Give the position of every malaria parasite.
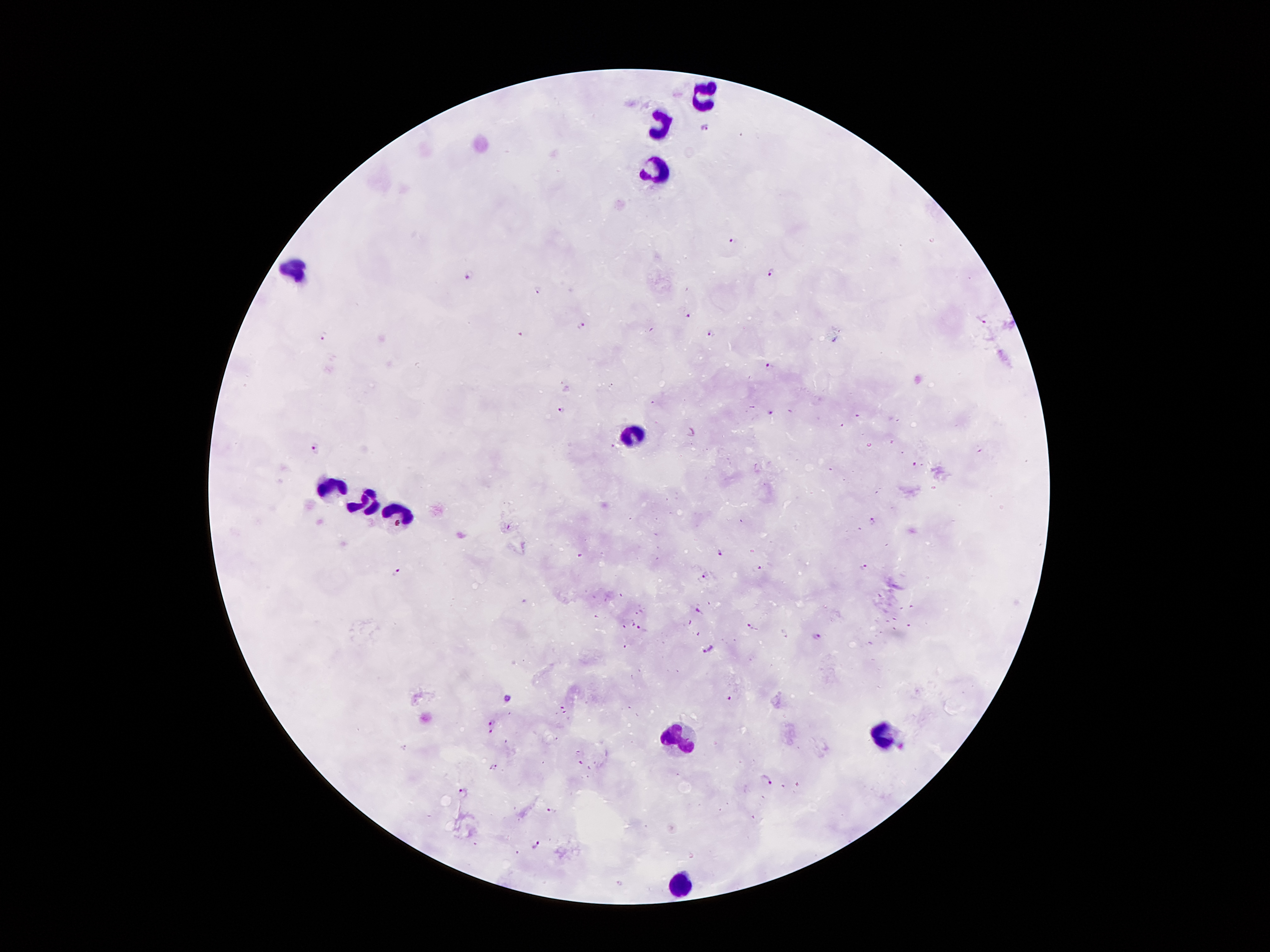

Approximate object centers, in pixels from the top-left corner.
Malaria parasites: (x=705, y=127), (x=736, y=240), (x=771, y=271), (x=467, y=274), (x=538, y=290), (x=691, y=317), (x=985, y=319), (x=582, y=324), (x=709, y=331), (x=519, y=333), (x=324, y=336), (x=770, y=365), (x=562, y=410), (x=771, y=410), (x=315, y=448), (x=915, y=464), (x=874, y=516), (x=719, y=553), (x=756, y=566), (x=862, y=567), (x=398, y=571), (x=705, y=575), (x=697, y=610), (x=752, y=628), (x=643, y=631), (x=814, y=637), (x=627, y=644), (x=708, y=649), (x=730, y=698), (x=507, y=700), (x=563, y=710), (x=494, y=726), (x=581, y=763), (x=493, y=767), (x=765, y=779), (x=461, y=791), (x=553, y=812), (x=535, y=844).

Leukocyte locations: (x=703, y=95), (x=658, y=125), (x=655, y=169), (x=296, y=270), (x=636, y=433), (x=332, y=486), (x=363, y=503), (x=397, y=517), (x=884, y=731), (x=673, y=735), (x=683, y=882). Giemsa-stained preparation. Single field of view. Image is 1270×952 pixels. 100x magnification. Patient malaria status: positive for Plasmodium falciparum. Smartphone photograph taken through the microscope eyepiece. Thick blood smear.